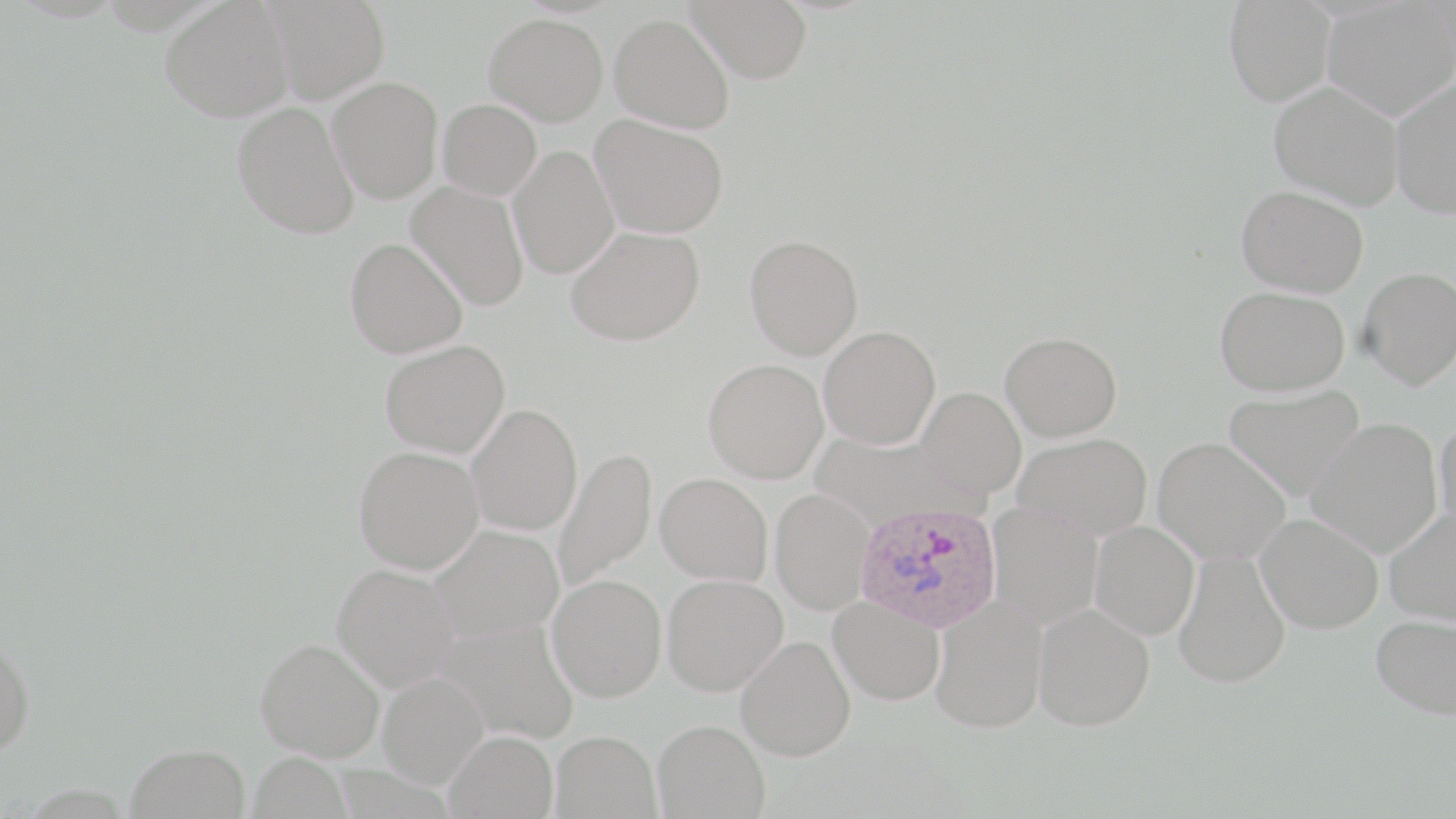
Summary:
  - Coordinate format: approximate bounding boxes as (x1,y1)-(x2,y2) corner pairs in pixels
  - Uninfected red blood cell locations: (160,0)-(293,122), (264,0)-(390,103), (687,0)-(814,83), (1322,0)-(1455,120), (1224,1)-(1335,106), (483,13)-(608,125), (609,13)-(735,134), (327,76)-(443,203), (1390,78)-(1456,219), (1268,80)-(1405,210), (437,99)-(542,200), (232,101)-(359,239), (590,114)-(728,238), (507,145)-(620,279), (406,181)-(530,311), (1237,184)-(1369,298), (566,225)-(705,346), (745,234)-(864,360), (345,238)-(468,358), (1358,267)-(1456,390), (1214,286)-(1350,396), (819,325)-(941,449), (1001,331)-(1123,442), (380,340)-(510,458), (703,358)-(829,483), (1223,384)-(1365,501), (916,386)-(1026,499), (466,403)-(582,536), (1434,414)-(1456,536), (1306,417)-(1443,558), (810,430)-(980,530), (1012,433)-(1153,541), (1153,436)-(1291,564), (354,445)-(484,573), (553,446)-(657,594), (656,472)-(773,586), (770,488)-(875,614), (987,503)-(1103,629), (1384,507)-(1456,626), (1256,512)-(1384,634), (1090,521)-(1199,640), (428,525)-(564,643), (1173,550)-(1291,688), (332,564)-(460,692), (661,573)-(788,696), (546,574)-(667,701), (829,595)-(945,705), (931,597)-(1048,734), (1033,603)-(1155,731), (1371,613)-(1456,720), (435,618)-(579,744), (735,636)-(855,761), (0,638)-(34,755), (256,638)-(384,761), (377,672)-(488,788), (653,719)-(770,818), (443,729)-(559,819), (549,730)-(661,818), (126,743)-(250,819), (248,752)-(353,819)
  - Plasmodium ovale-infected red blood cell locations: (855,501)-(1002,633)
  - Slide-level diagnosis: Plasmodium ovale
  - Stain: May-Grünwald-Giemsa
  - Magnification: 1000x
  - Modality: light microscopy
  - Image size: 1456×819 pixels
  - Preparation: thin blood film
  - Field of view: single